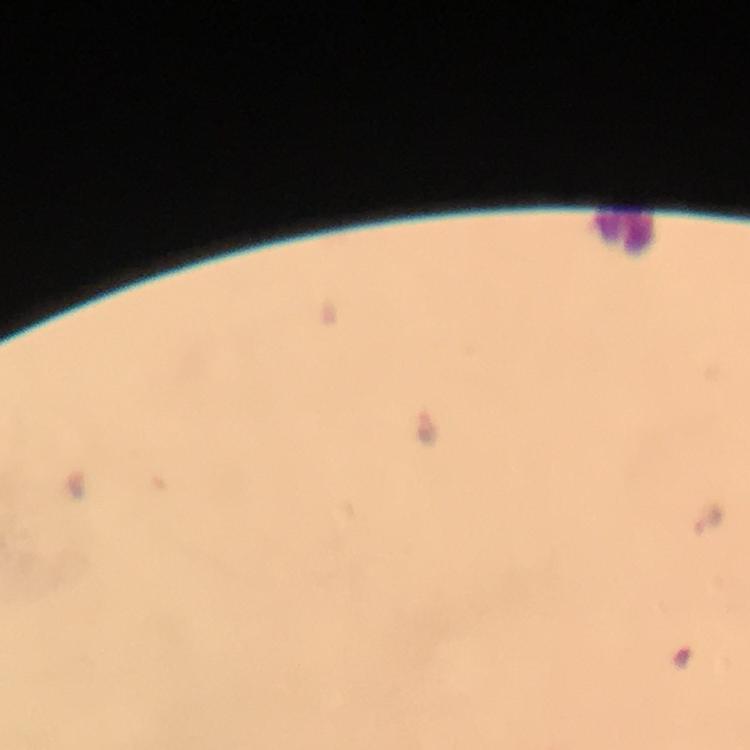
{
  "leukocyte_locations": "approximate centers as {x, y} in pixels: {622, 230}",
  "stain": "Giemsa",
  "context": "from a malaria diagnostic workup",
  "cropped_from": "one field of view",
  "image_size": "750×750 pixels",
  "preparation": "thick blood smear",
  "magnification": "100x",
  "capture": "smartphone mounted on the microscope",
  "plasmodium_parasite_locations": "approximate centers as {x, y} in pixels: {428, 427}",
  "immersion_oil": "used"
}